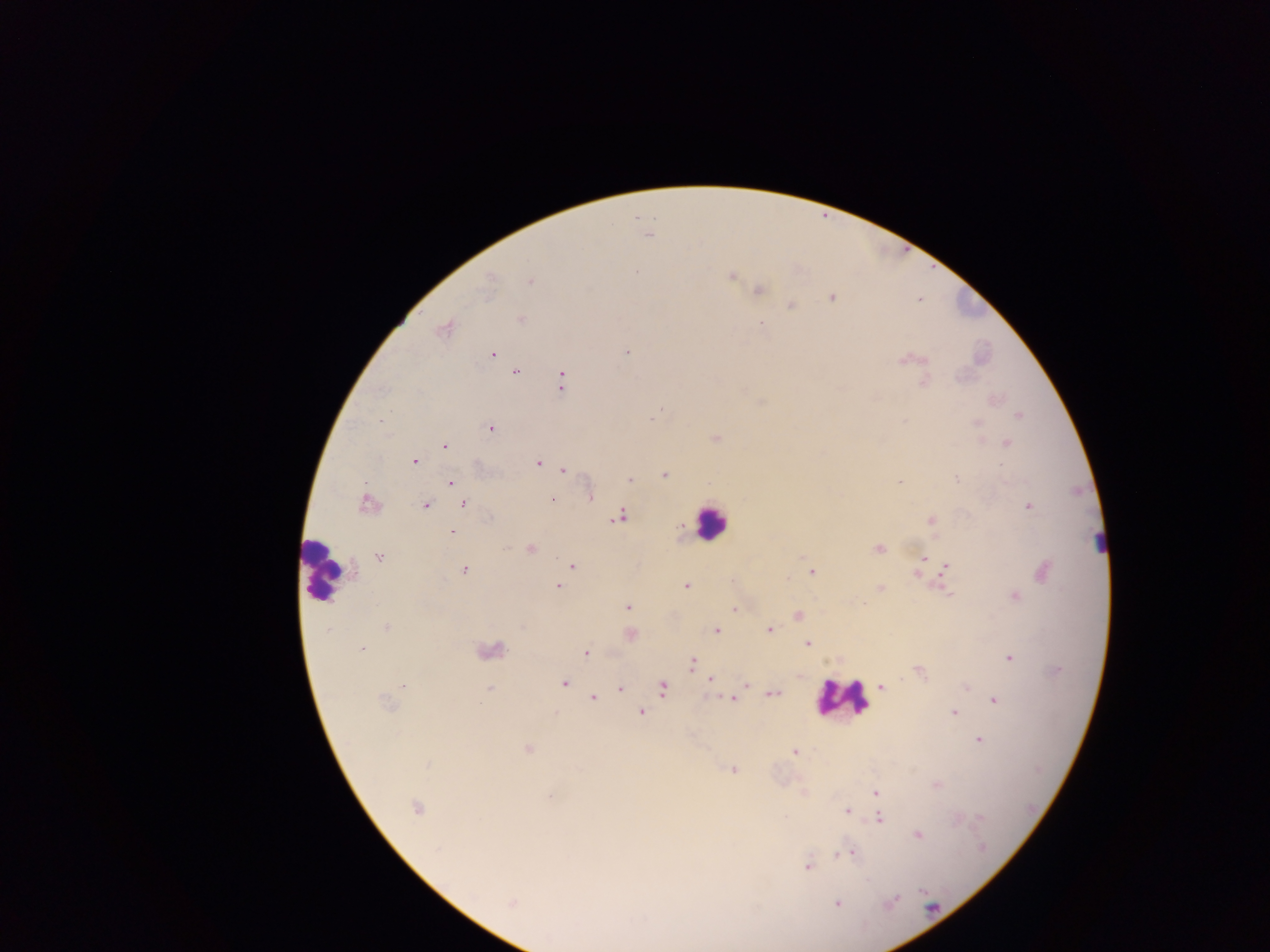 Approximate centers as {x, y} in pixels. Malaria parasite locations: {649, 235}, {636, 271}, {731, 276}, {531, 281}, {488, 283}, {759, 291}, {832, 298}, {792, 305}, {521, 318}, {761, 324}, {444, 328}, {627, 352}, {493, 354}, {905, 359}, {515, 372}, {561, 381}, {924, 382}, {661, 410}, {658, 413}, {1018, 415}, {653, 417}, {380, 421}, {904, 421}, {977, 423}, {491, 428}, {716, 437}, {1007, 442}, {444, 446}, {415, 461}, {538, 463}, {563, 469}, {665, 475}, {956, 478}, {629, 479}, {451, 482}, {898, 482}, {590, 497}, {552, 499}, {464, 504}, {367, 505}, {426, 506}, {1029, 507}, {619, 517}, {931, 521}, {452, 532}, {529, 548}, {878, 548}, {380, 557}, {925, 558}, {572, 565}, {946, 567}, {465, 570}, {812, 572}, {1044, 572}, {916, 574}, {557, 586}, {685, 586}, {880, 588}, {948, 594}, {1015, 596}, {628, 608}, {734, 609}, {797, 616}, {386, 627}, {329, 629}, {769, 630}, {716, 631}, {631, 635}, {807, 643}, {361, 650}, {586, 652}, {1009, 658}, {692, 663}, {918, 671}, {710, 680}, {564, 683}, {744, 684}, {403, 685}, {881, 687}, {966, 687}, {620, 688}, {663, 688}, {489, 689}, {773, 693}, {593, 698}, {732, 698}, {994, 700}, {386, 704}, {479, 704}, {954, 712}, {641, 713}, {979, 740}, {527, 749}, {794, 753}, {428, 764}, {733, 769}, {936, 785}, {875, 792}, {550, 796}, {415, 807}, {847, 810}, {880, 818}, {981, 818}, {918, 834}, {847, 853}, {838, 855}, {807, 866}, {893, 901}, {511, 903}, {837, 904}. Leukocyte locations: {970, 303}, {710, 521}, {322, 568}, {842, 698}. Mobile-phone photograph taken through the microscope. Image is 1270×952 pixels. Thick blood film. Collected in Ghana. One field of view.